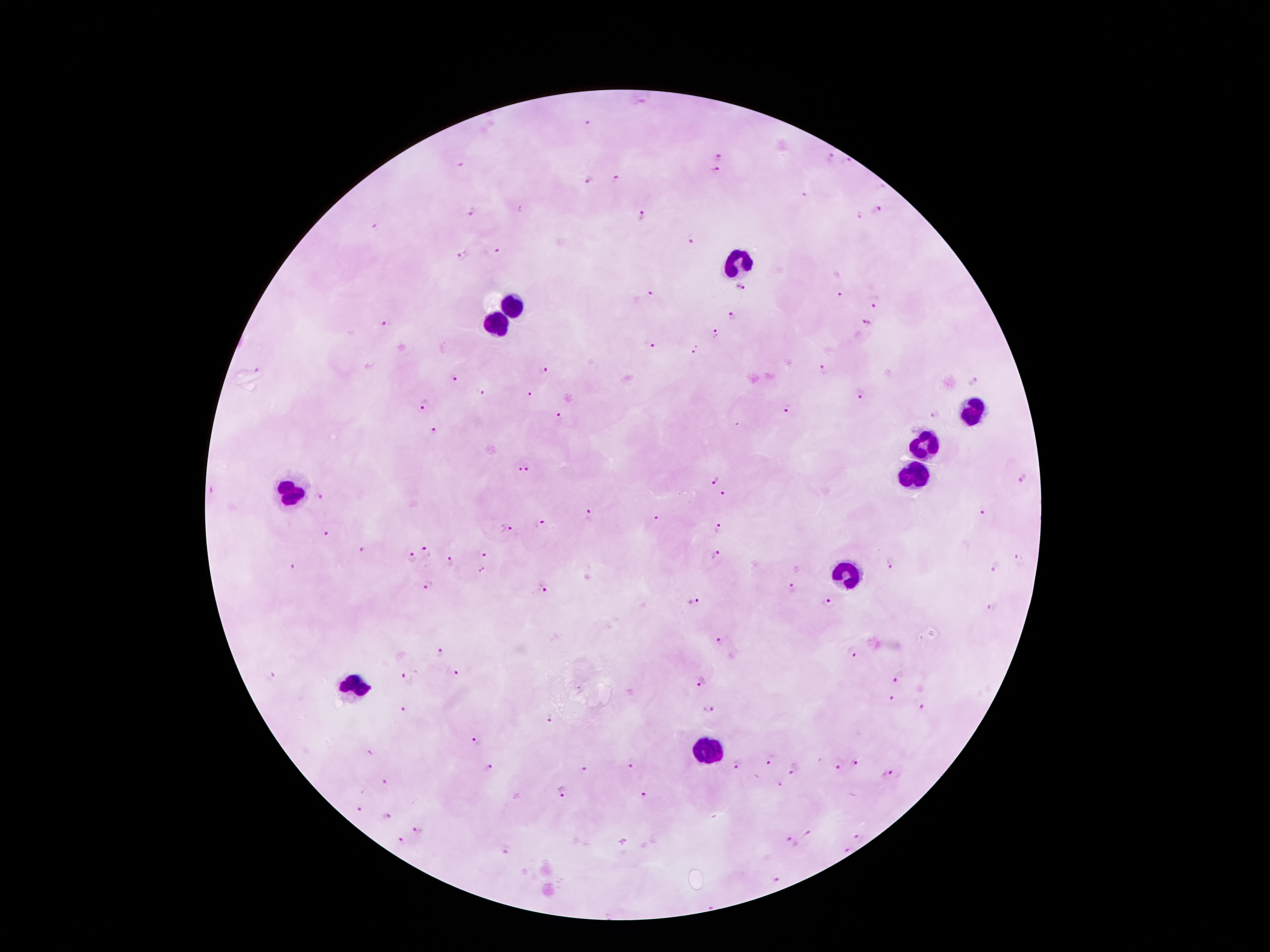

Approximate centers as {x, y} in pixels.
Summary:
  - Malaria parasite locations: {641, 100}, {587, 121}, {830, 155}, {718, 156}, {461, 162}, {847, 162}, {715, 171}, {585, 179}, {617, 180}, {805, 196}, {878, 211}, {473, 212}, {642, 215}, {861, 216}, {376, 227}, {691, 239}, {497, 252}, {462, 255}, {742, 287}, {652, 291}, {843, 294}, {875, 300}, {732, 318}, {866, 323}, {386, 326}, {714, 334}, {648, 344}, {696, 350}, {544, 368}, {258, 370}, {821, 371}, {453, 377}, {971, 383}, {481, 391}, {528, 393}, {859, 393}, {424, 404}, {787, 409}, {935, 415}, {559, 416}, {435, 431}, {518, 468}, {530, 468}, {1022, 477}, {715, 482}, {723, 494}, {321, 498}, {982, 510}, {590, 515}, {654, 519}, {541, 525}, {506, 528}, {718, 529}, {325, 534}, {362, 549}, {428, 552}, {716, 554}, {485, 556}, {1019, 557}, {412, 559}, {451, 562}, {890, 563}, {993, 566}, {294, 568}, {484, 570}, {428, 585}, {544, 586}, {792, 587}, {694, 604}, {829, 604}, {992, 608}, {721, 640}, {440, 653}, {852, 653}, {453, 673}, {406, 674}, {271, 675}, {899, 678}, {700, 684}, {892, 699}, {708, 708}, {924, 709}, {404, 710}, {550, 718}, {476, 741}, {771, 761}, {856, 763}, {839, 764}, {631, 766}, {737, 766}, {587, 768}, {490, 769}, {794, 769}, {886, 773}, {387, 782}, {780, 787}, {562, 792}, {645, 797}, {360, 809}, {389, 816}, {419, 831}, {808, 834}, {859, 838}, {402, 841}, {791, 843}, {506, 851}, {847, 851}, {778, 880}
  - Leukocyte locations: {742, 262}, {512, 307}, {496, 322}, {975, 410}, {925, 443}, {914, 477}, {292, 491}, {846, 575}, {355, 685}, {709, 747}
  - Capture: smartphone through the microscope eyepiece
  - Patient malaria status: infected with Plasmodium falciparum
  - Magnification: 100x
  - Image size: 1270×952 pixels
  - Preparation: thick peripheral-blood smear
  - Stain: Giemsa
  - Field of view: single